Locate and identify every blood parasite.
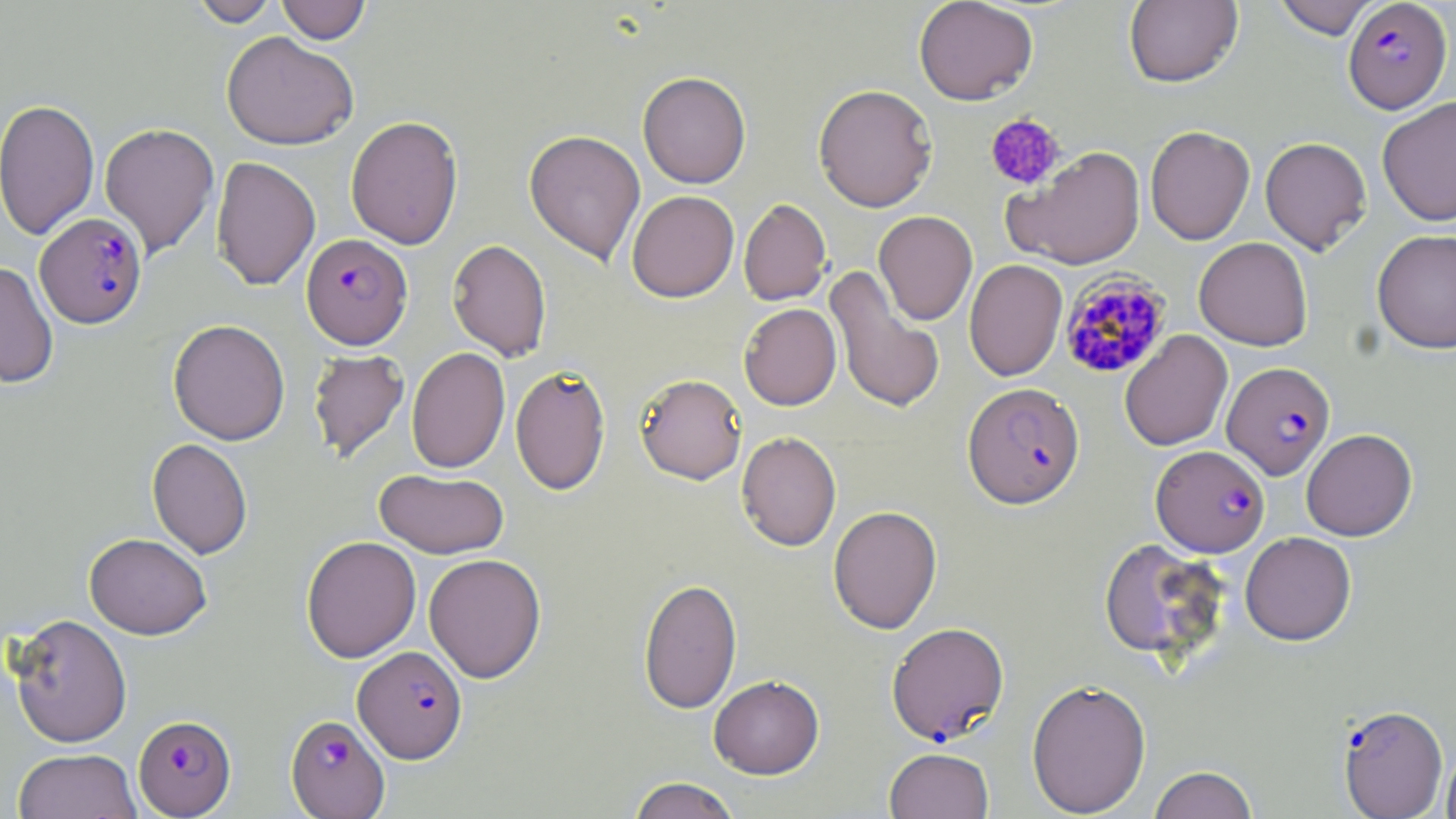
Approximate bounding boxes as (x1,y1)-(x2,y2) corner pairs in pixels.
Plasmodium falciparum-infected red blood cells: (1342,0)-(1452,114), (34,212)-(147,328), (302,233)-(412,349), (1059,270)-(1172,380), (1222,361)-(1336,480), (962,382)-(1085,509), (1151,444)-(1269,557), (886,622)-(1009,745), (353,645)-(467,762), (1338,703)-(1448,818), (285,714)-(390,818), (134,715)-(236,817).
No Plasmodium ovale, Plasmodium malariae, Plasmodium vivax, Babesia divergens, or Trypanosoma brucei observed.

Summary:
  - Platelet locations: (984,112)-(1066,192)
  - Uninfected red blood cell locations: (190,0)-(280,27), (276,0)-(371,44), (913,0)-(1039,105), (1123,0)-(1243,88), (1271,0)-(1383,39), (221,31)-(358,150), (638,71)-(751,188), (813,83)-(938,212), (1377,97)-(1456,225), (0,98)-(100,240), (345,115)-(463,249), (99,122)-(220,258), (1145,126)-(1255,244), (524,129)-(646,266), (1260,136)-(1372,255), (1005,146)-(1146,270), (210,156)-(320,290), (627,190)-(739,302), (739,198)-(832,306), (874,210)-(978,325), (1371,228)-(1456,354), (1194,237)-(1313,350), (447,239)-(552,361), (964,259)-(1067,382), (0,261)-(59,389), (825,267)-(945,414), (739,303)-(841,410), (168,319)-(290,445), (1119,330)-(1233,451), (406,346)-(510,473), (308,348)-(410,463), (510,365)-(611,495), (635,373)-(748,485), (1301,428)-(1417,541), (736,431)-(841,551), (147,439)-(253,558), (374,468)-(508,559), (828,505)-(942,634), (1240,532)-(1357,646), (84,533)-(212,639), (301,535)-(421,662), (1098,538)-(1229,662), (423,553)-(546,683), (637,577)-(743,712), (6,613)-(133,747), (709,674)-(825,779), (1026,678)-(1151,818), (1441,743)-(1456,819), (884,747)-(993,819), (13,748)-(142,819), (1149,765)-(1258,819), (627,776)-(742,819)
  - Slide-level diagnosis: Plasmodium falciparum
  - Magnification: 1000x
  - Modality: light microscopy
  - Image size: 1456×819 pixels
  - Stain: May-Grünwald-Giemsa
  - Field of view: one of a larger specimen
  - Preparation: thin blood smear